Comment on the morphology of the erythrocytes.
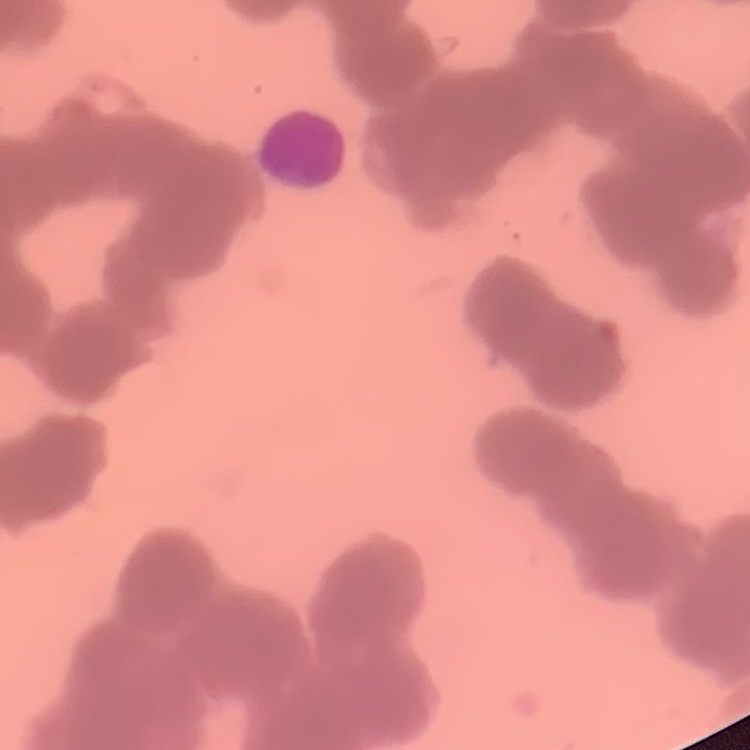

Rouleaux formation.

Square crop of a larger photomicrograph. Stained with either Field's or Giemsa. Thin blood film.